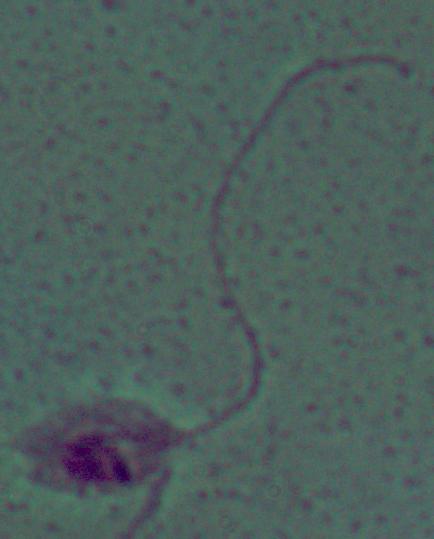

Summary:
  - Modality: photomicrograph
  - Identification: Leishmania
  - Magnification: 1000x